Identify the cell.
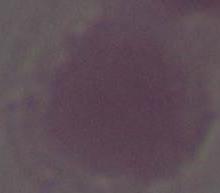
This is an erythrocyte.

Summary:
  - Magnification: 1000x
  - Modality: photomicrograph